Report the malaria status of this cell.
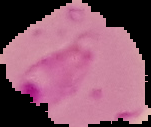

It is parasitized.

Summary:
  - Image type: segmented cell region with the area outside set to black
  - Preparation: thin blood smear
  - Image size: 151×127 pixels